Classify this cell by malaria status.
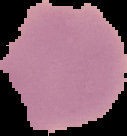

It is uninfected.

{
  "image_size": "127×136 pixels",
  "preparation": "thin blood film",
  "image_type": "segmented cell region with the area outside set to black"
}